Name the parasite shown.
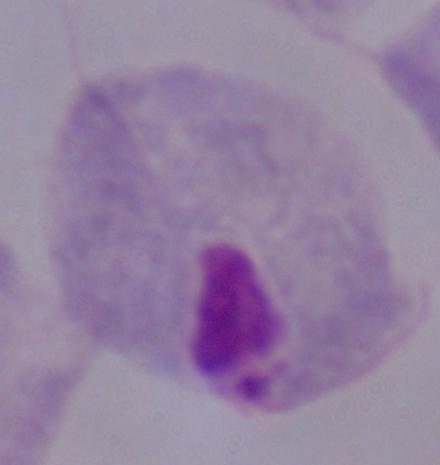

This is a trichomonad.

modality = photomicrograph
magnification = 1000x